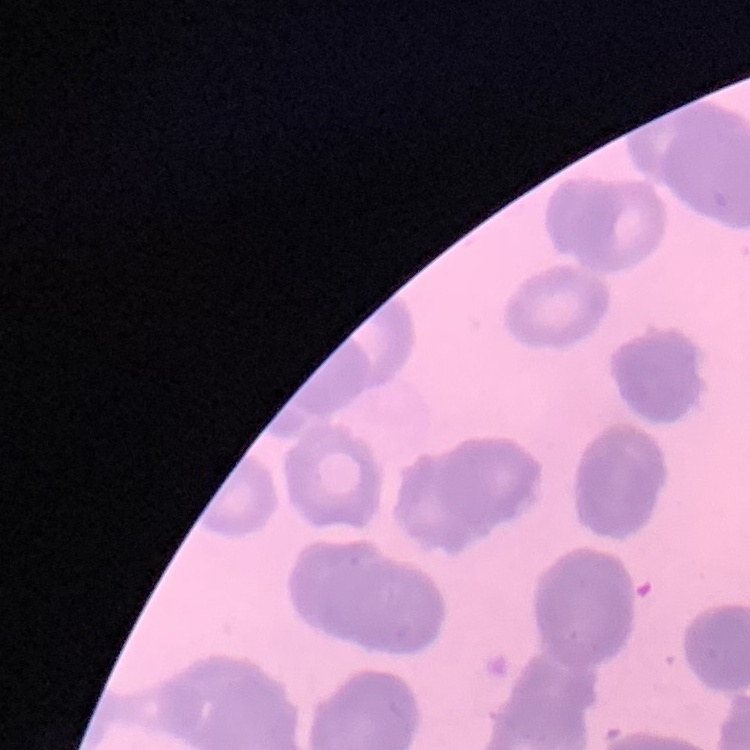
Summary:
  - Erythrocyte morphology: rouleaux formation
  - Preparation: thin blood film
  - Stain: Field's or Giemsa
  - Image type: square crop of a larger photomicrograph